Identify the parasite.
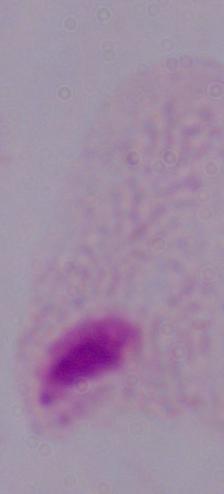
A trichomonad.

magnification = 1000x
modality = micrograph